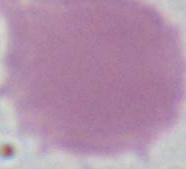

modality = micrograph
magnification = 1000x
identification = red blood cell